Report the malaria status of this cell.
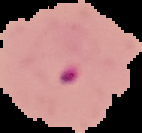
Parasitized.

The area outside the segmented cell region is set to black. From a thin blood film. Image is 142×133 pixels.